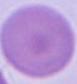
Summary:
  - Magnification: 1000x
  - Identification: erythrocyte
  - Modality: micrograph